Report the malaria status of this cell.
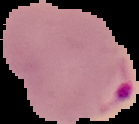

Parasitized.

Summary:
  - Image size: 139×124 pixels
  - Image type: segmented cell region on a black background
  - Preparation: thin blood film